Comment on the morphology of the red blood cells.
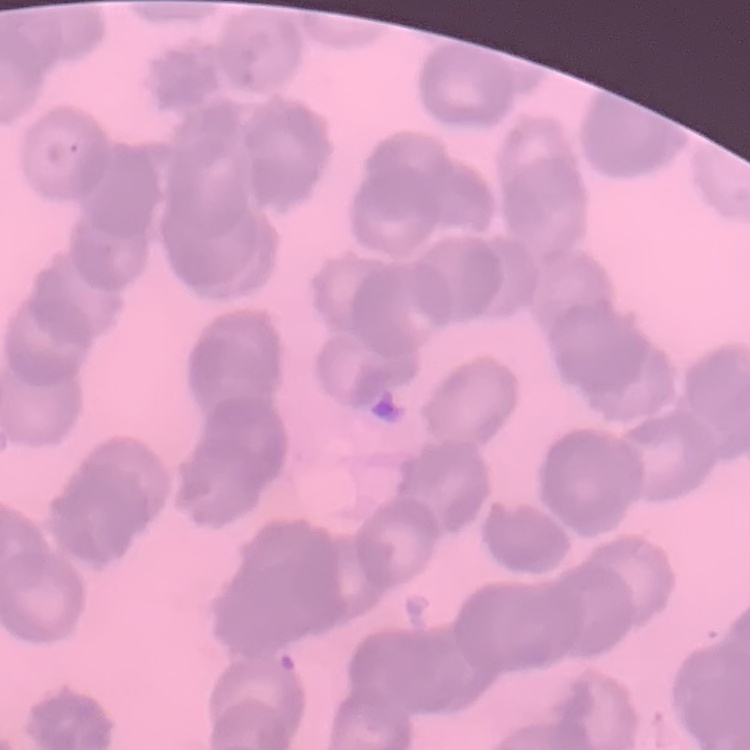
Rouleaux formation.

Summary:
  - Image type: one tile cut from a larger photomicrograph
  - Preparation: thin blood film
  - Stain: Field's or Giemsa